Report the malaria status of this cell.
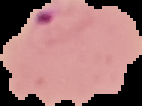

It is parasitized.

Summary:
  - Preparation: thin blood smear
  - Image size: 142×106 pixels
  - Image type: segmented cell region on a black background